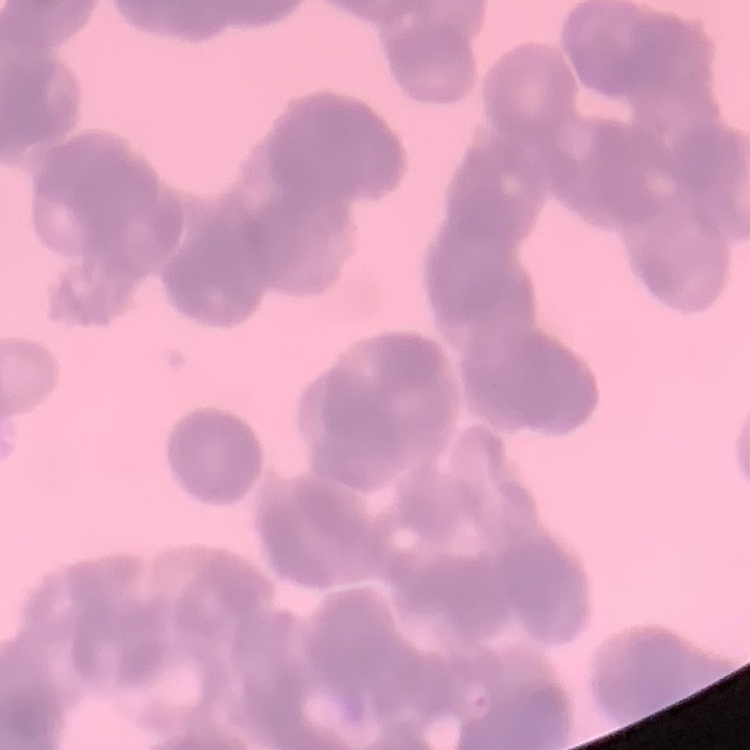
The erythrocytes exhibit rouleaux formation. One tile cut from a larger photomicrograph. Field's or Giemsa stain. Thin blood smear.